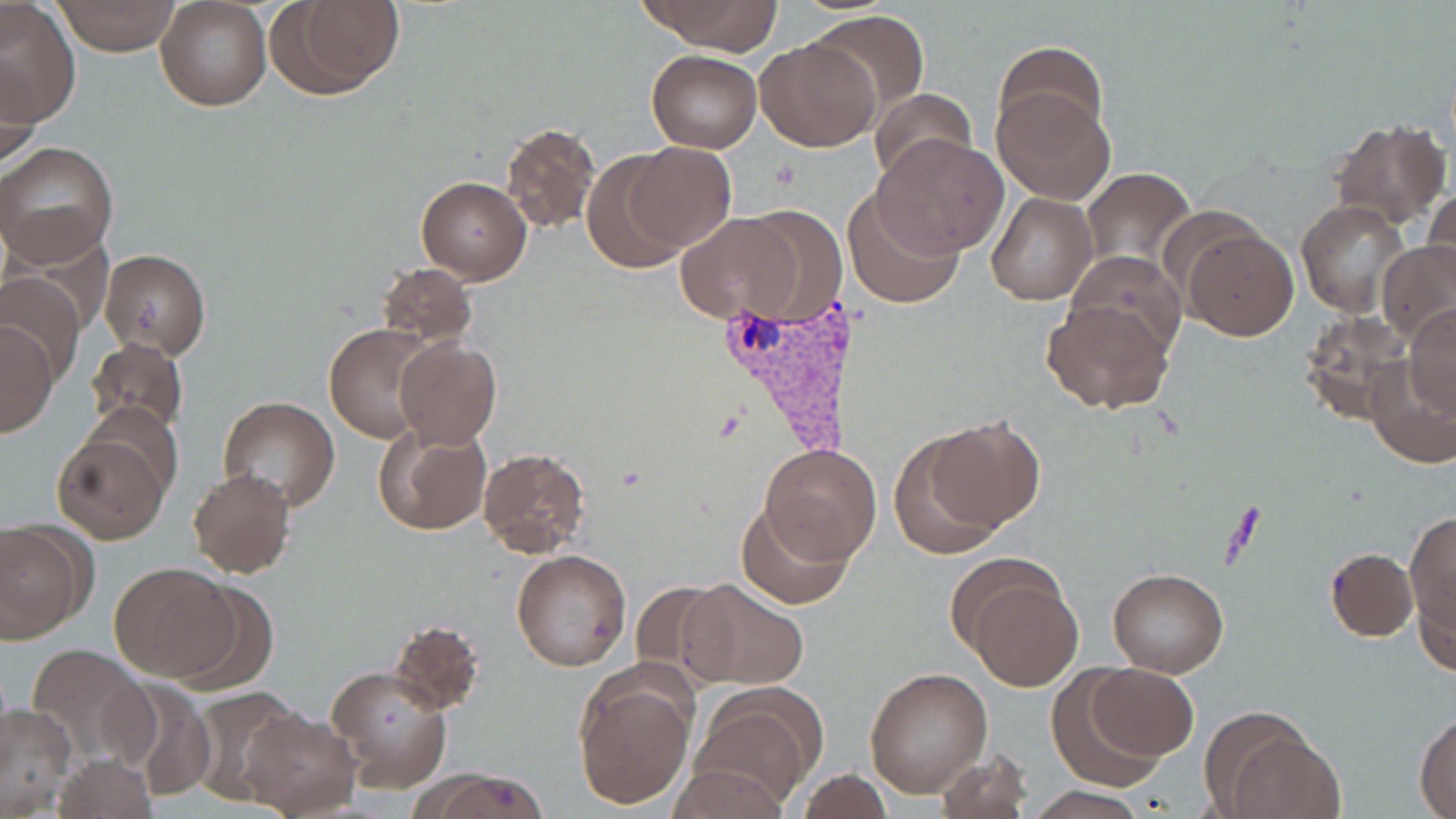 Approximate bounding boxes as [x1, y1, x2, y2] in pixels. Plasmodium vivax-infected red blood cell locations: [720, 295, 860, 465]. Platelet locations: [771, 159, 803, 193]. Uninfected red blood cell locations: [0, 0, 80, 126], [55, 0, 181, 54], [155, 0, 271, 110], [639, 0, 782, 52], [264, 1, 407, 100], [810, 9, 930, 114], [756, 34, 880, 151], [994, 41, 1107, 140], [646, 50, 761, 153], [1, 62, 42, 168], [870, 88, 974, 188], [993, 88, 1113, 205], [1328, 118, 1452, 232], [500, 122, 600, 233], [872, 134, 1010, 257], [0, 141, 119, 266], [624, 142, 734, 251], [581, 151, 695, 273], [1078, 166, 1196, 275], [416, 175, 531, 285], [1421, 185, 1455, 295], [843, 188, 965, 310], [986, 193, 1096, 305], [1297, 201, 1411, 318], [735, 207, 849, 324], [675, 213, 803, 325], [4, 223, 118, 334], [1179, 226, 1298, 340], [1378, 239, 1456, 347], [99, 248, 211, 360], [1067, 250, 1186, 361], [375, 262, 478, 348], [0, 270, 86, 382], [1041, 300, 1175, 416], [1405, 305, 1456, 424], [1298, 311, 1415, 426], [0, 321, 58, 438], [325, 323, 441, 443], [85, 337, 191, 439], [393, 337, 501, 448], [1365, 358, 1456, 469], [85, 395, 184, 497], [218, 398, 341, 513], [924, 415, 1045, 532], [372, 423, 492, 537], [52, 430, 170, 544], [888, 431, 1007, 558], [762, 443, 880, 563], [477, 447, 592, 559], [188, 468, 297, 578], [735, 500, 853, 611], [1404, 508, 1456, 657], [0, 519, 93, 641], [511, 548, 633, 672], [1324, 548, 1417, 642], [953, 559, 1085, 690], [109, 561, 240, 681], [1107, 568, 1229, 676], [679, 576, 808, 690], [166, 577, 282, 691], [627, 580, 740, 685], [388, 619, 485, 715], [23, 644, 154, 770], [1085, 663, 1199, 761], [325, 664, 452, 789], [864, 666, 992, 799], [574, 669, 696, 809], [1047, 671, 1167, 785], [105, 678, 217, 801], [689, 684, 821, 809], [184, 688, 303, 805], [0, 702, 78, 816], [236, 707, 362, 816], [1202, 711, 1341, 818], [1415, 712, 1456, 816], [934, 747, 1033, 819], [51, 756, 155, 817], [668, 763, 788, 818], [417, 767, 552, 819], [793, 771, 898, 817], [1028, 787, 1146, 817]. Slide-level diagnosis: Plasmodium vivax. Single field of view. Captured at 1000x magnification. May-Grünwald-Giemsa stain. Image is 1456×819 pixels. Thin blood film. Optical microscopy.